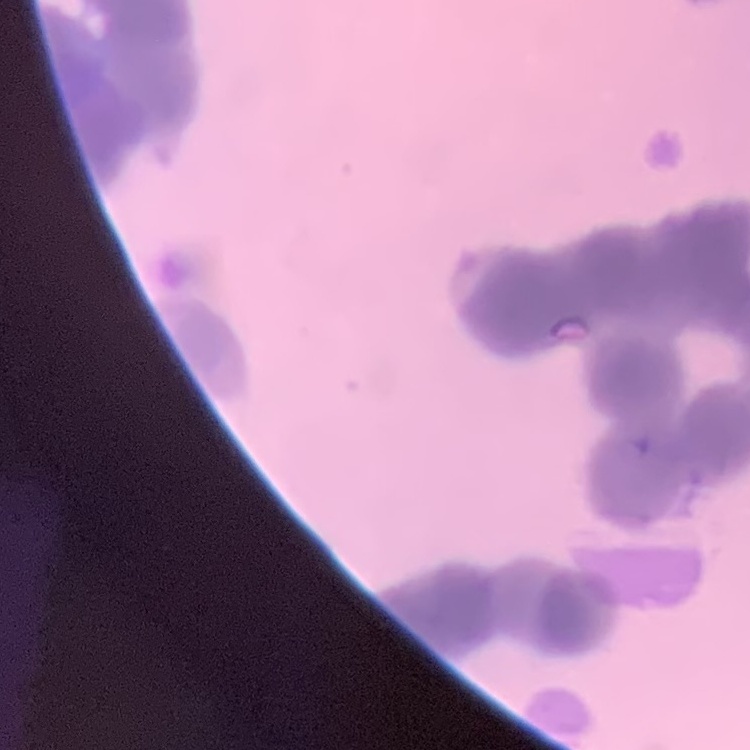
The erythrocytes show rouleaux formation. Thin peripheral smear. Field's or Giemsa stain. One tile cut from a larger photomicrograph.